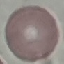 Malaria status: uninfected. Giemsa-stained preparation. Thin blood smear. Cell patch, automatically extracted from a larger field of view and resized to 64 × 64 pixels. Acquired by smartphone through the microscope eyepiece.